Locate and identify every blood parasite.
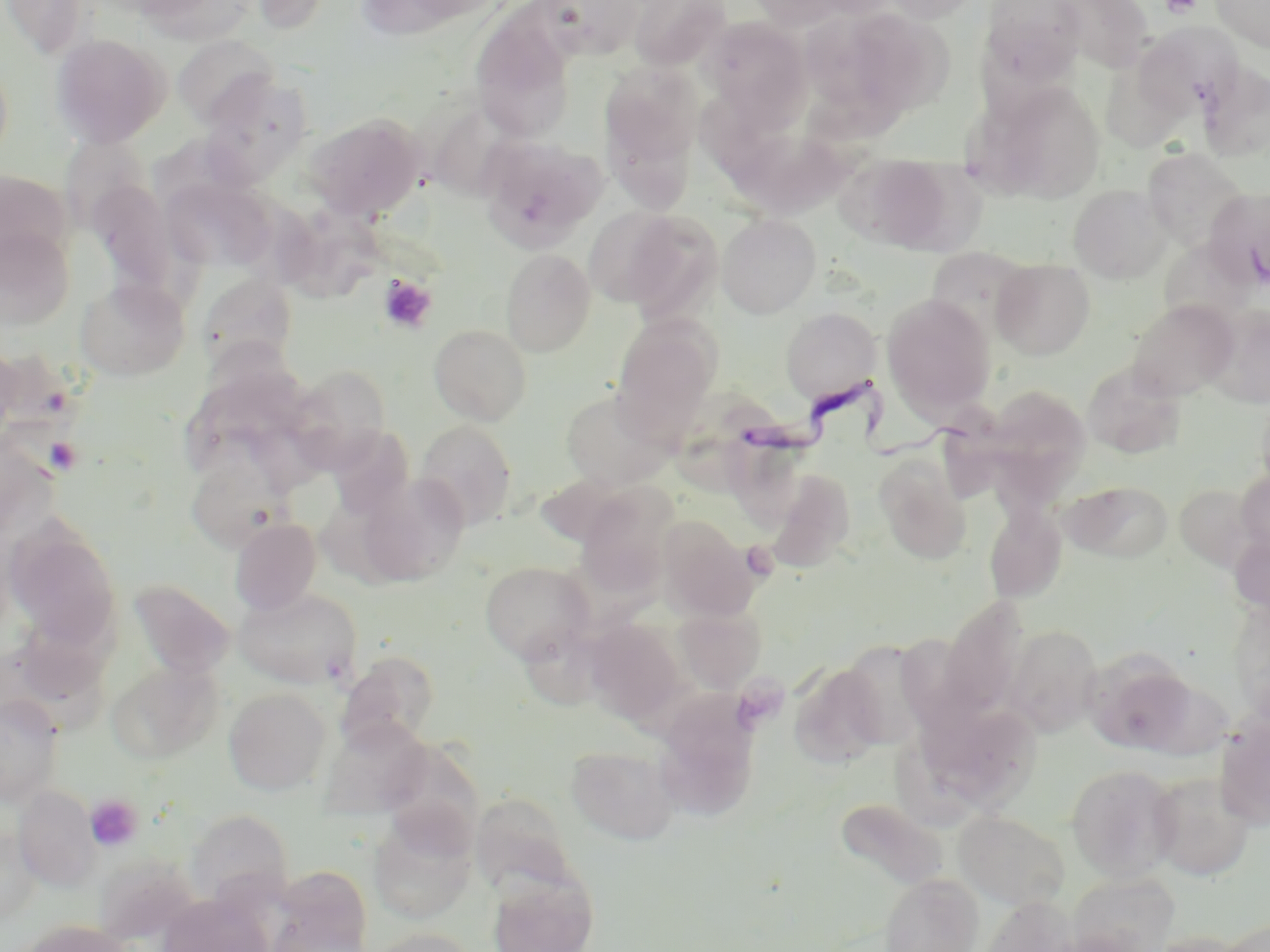

Approximate bounding boxes as [x1, y1, x2, y2] in pixels.
Trypanosoma brucei: [738, 367, 985, 470].
No Plasmodium falciparum, Plasmodium ovale, Plasmodium malariae, Plasmodium vivax, or Babesia divergens observed.

slide-level diagnosis = Trypanosoma brucei
field of view = single
platelet locations = approximate bounding boxes as [x1, y1, x2, y2] in pixels: [1162, 0, 1202, 18], [378, 275, 437, 333], [43, 436, 84, 475], [86, 794, 142, 851]
uninfected red blood cell locations = approximate bounding boxes as [x1, y1, x2, y2] in pixels: [1, 0, 92, 59], [533, 0, 647, 60], [628, 0, 732, 71], [746, 0, 858, 30], [880, 0, 984, 24], [980, 0, 1085, 89], [1052, 0, 1152, 73], [1212, 0, 1270, 52], [139, 1, 259, 45], [805, 4, 944, 122], [471, 11, 576, 144], [698, 17, 811, 122], [1135, 23, 1244, 121], [51, 33, 171, 147], [173, 35, 280, 128], [599, 64, 702, 197], [1199, 64, 1269, 162], [975, 79, 1106, 203], [424, 103, 518, 200], [307, 114, 425, 222], [58, 135, 152, 229], [479, 135, 605, 252], [724, 138, 881, 215], [1143, 148, 1247, 251], [840, 152, 956, 253], [0, 169, 72, 268], [162, 177, 278, 273], [87, 179, 180, 292], [1069, 184, 1171, 283], [271, 206, 398, 299], [583, 207, 688, 308], [615, 210, 724, 323], [717, 213, 821, 317], [0, 226, 75, 330], [933, 246, 1028, 341], [500, 248, 596, 357], [992, 258, 1095, 360], [196, 272, 298, 375], [75, 277, 190, 381], [881, 293, 996, 419], [1127, 299, 1238, 401], [1203, 303, 1270, 407], [781, 307, 881, 405], [610, 314, 721, 440], [429, 325, 532, 426], [0, 342, 22, 444], [1082, 362, 1186, 459], [288, 364, 392, 470], [984, 385, 1091, 484], [560, 388, 675, 490], [415, 420, 518, 530], [328, 426, 415, 520], [186, 451, 295, 552], [875, 456, 972, 564], [766, 469, 857, 571], [1235, 471, 1270, 557], [358, 474, 469, 586], [1062, 480, 1173, 563], [576, 484, 680, 596], [1173, 484, 1257, 571], [984, 500, 1067, 604], [657, 515, 756, 620], [230, 518, 321, 615], [4, 523, 122, 651], [1229, 529, 1270, 619], [479, 561, 594, 663], [129, 579, 235, 680], [232, 587, 362, 689], [938, 597, 1029, 720], [673, 604, 766, 694], [584, 617, 688, 725], [1004, 625, 1104, 735], [515, 628, 626, 720], [898, 628, 987, 740], [847, 639, 935, 745], [337, 650, 440, 751], [1087, 651, 1199, 754], [108, 659, 224, 763], [790, 663, 886, 768], [224, 688, 331, 795], [654, 691, 762, 822], [0, 694, 65, 806], [1215, 714, 1270, 830], [319, 718, 432, 820], [933, 720, 1047, 809], [566, 745, 680, 845], [1066, 763, 1183, 881], [1148, 772, 1256, 880], [13, 784, 101, 890], [469, 793, 578, 901], [834, 797, 948, 892], [186, 809, 294, 907], [954, 810, 1070, 910], [369, 814, 476, 923], [1, 826, 41, 923], [268, 867, 373, 952], [488, 872, 598, 952], [1067, 872, 1180, 952], [879, 873, 983, 952], [160, 893, 271, 952], [977, 896, 1079, 952], [17, 919, 132, 952], [1218, 919, 1270, 952], [367, 927, 479, 952], [1146, 931, 1252, 952]
image size = 1270×952 pixels
modality = optical microscopy
preparation = thin blood film
magnification = 1000x
stain = May-Grünwald-Giemsa